Name the parasite shown.
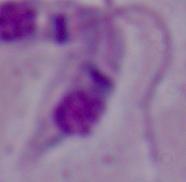

Leishmania.

Summary:
  - Magnification: 1000x
  - Modality: photomicrograph